Assess this cell for malaria.
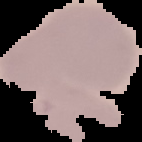

Uninfected.

{
  "image_type": "segmented cell region with the area outside set to black",
  "preparation": "thin blood film",
  "image_size": "142×142 pixels"
}